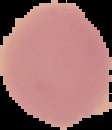 Result: negative for malaria parasites. From a thin blood smear. Image is 112×130 pixels. Segmented cell region on a black background.